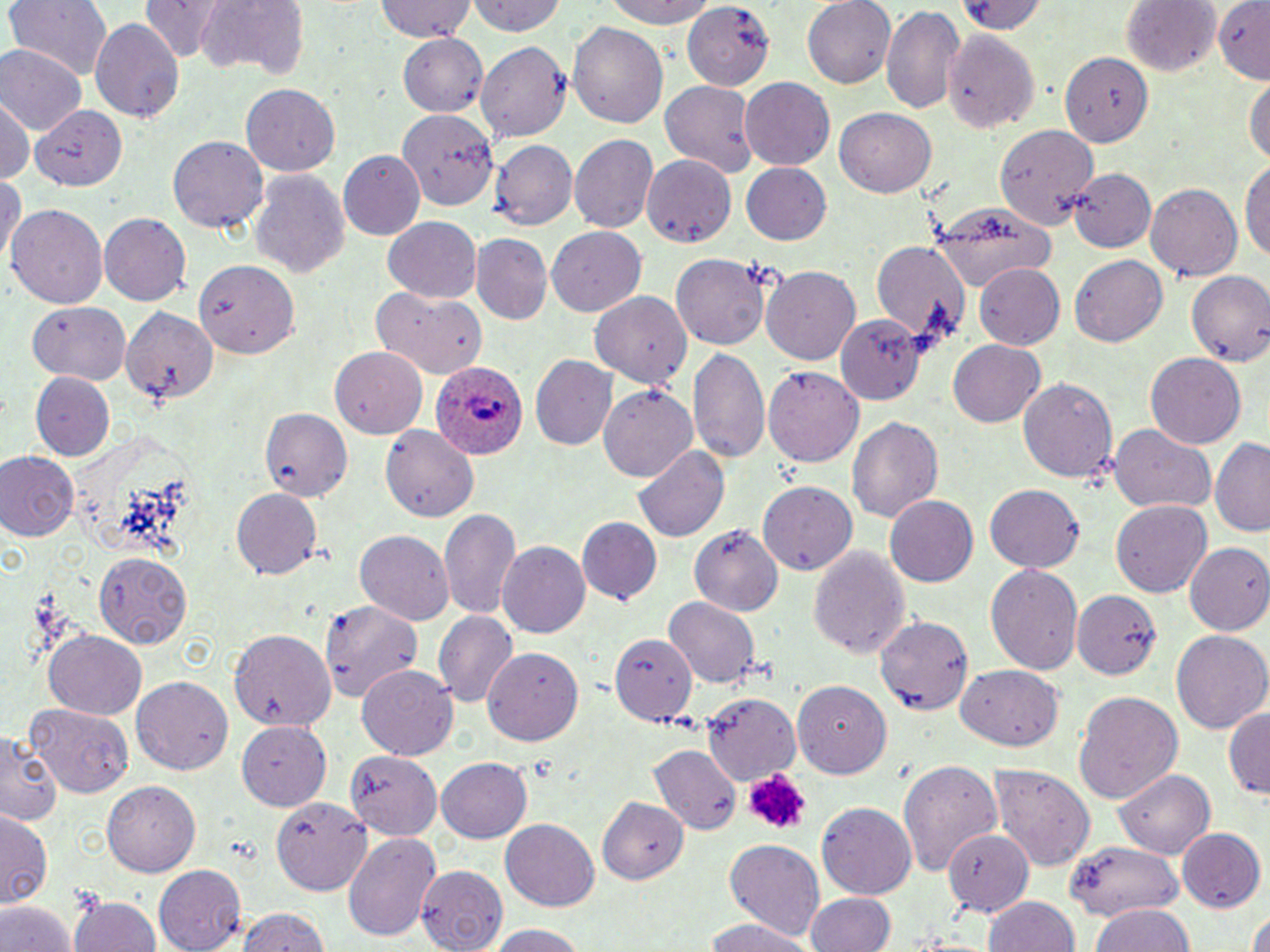

Summary:
  - Coordinate format: approximate bounding boxes as named x1/y1/x2/y2 corners in pixels
  - Plasmodium ovale-infected red blood cell locations: (x1=428, y1=355, x2=528, y2=462)
  - Platelet locations: (x1=739, y1=767, x2=811, y2=835)
  - Uninfected red blood cell locations: (x1=3, y1=0, x2=111, y2=81), (x1=373, y1=0, x2=477, y2=43), (x1=597, y1=0, x2=726, y2=28), (x1=802, y1=0, x2=896, y2=89), (x1=957, y1=0, x2=1053, y2=36), (x1=1212, y1=0, x2=1270, y2=82), (x1=468, y1=1, x2=570, y2=38), (x1=682, y1=1, x2=771, y2=87), (x1=1121, y1=1, x2=1218, y2=78), (x1=142, y1=2, x2=226, y2=61), (x1=193, y1=3, x2=303, y2=80), (x1=880, y1=6, x2=966, y2=116), (x1=90, y1=17, x2=184, y2=125), (x1=569, y1=20, x2=668, y2=130), (x1=942, y1=24, x2=1040, y2=131), (x1=399, y1=36, x2=491, y2=114), (x1=479, y1=42, x2=572, y2=142), (x1=0, y1=45, x2=83, y2=136), (x1=1055, y1=47, x2=1155, y2=150), (x1=1246, y1=73, x2=1269, y2=174), (x1=739, y1=77, x2=833, y2=167), (x1=662, y1=80, x2=757, y2=178), (x1=241, y1=82, x2=342, y2=174), (x1=0, y1=96, x2=33, y2=184), (x1=31, y1=103, x2=128, y2=189), (x1=399, y1=106, x2=498, y2=214), (x1=834, y1=109, x2=936, y2=198), (x1=992, y1=123, x2=1099, y2=234), (x1=568, y1=136, x2=656, y2=234), (x1=168, y1=137, x2=268, y2=235), (x1=490, y1=140, x2=576, y2=229), (x1=339, y1=150, x2=427, y2=240), (x1=644, y1=157, x2=737, y2=245), (x1=1241, y1=160, x2=1269, y2=261), (x1=740, y1=161, x2=832, y2=244), (x1=1068, y1=166, x2=1157, y2=251), (x1=0, y1=171, x2=24, y2=270), (x1=249, y1=171, x2=349, y2=279), (x1=1147, y1=182, x2=1242, y2=283), (x1=929, y1=201, x2=1055, y2=288), (x1=7, y1=203, x2=108, y2=308), (x1=100, y1=212, x2=194, y2=305), (x1=384, y1=217, x2=482, y2=303), (x1=546, y1=227, x2=644, y2=316), (x1=472, y1=234, x2=551, y2=324), (x1=870, y1=238, x2=969, y2=347), (x1=1070, y1=252, x2=1168, y2=344), (x1=673, y1=254, x2=770, y2=349), (x1=196, y1=262, x2=301, y2=360), (x1=975, y1=265, x2=1065, y2=350), (x1=760, y1=266, x2=861, y2=365), (x1=1186, y1=270, x2=1270, y2=367), (x1=590, y1=291, x2=692, y2=386), (x1=382, y1=293, x2=489, y2=381), (x1=29, y1=300, x2=130, y2=383), (x1=118, y1=305, x2=216, y2=414), (x1=831, y1=315, x2=923, y2=402), (x1=948, y1=340, x2=1045, y2=428), (x1=328, y1=347, x2=427, y2=438), (x1=688, y1=348, x2=768, y2=462), (x1=1144, y1=352, x2=1247, y2=450), (x1=532, y1=355, x2=618, y2=452), (x1=765, y1=366, x2=864, y2=467), (x1=30, y1=373, x2=115, y2=461), (x1=1018, y1=377, x2=1118, y2=485), (x1=599, y1=383, x2=699, y2=482), (x1=262, y1=405, x2=357, y2=502), (x1=846, y1=416, x2=943, y2=528), (x1=382, y1=423, x2=480, y2=523), (x1=1109, y1=426, x2=1218, y2=515), (x1=1211, y1=436, x2=1270, y2=538), (x1=633, y1=445, x2=729, y2=543), (x1=0, y1=450, x2=79, y2=541), (x1=758, y1=480, x2=859, y2=576), (x1=986, y1=484, x2=1085, y2=573), (x1=231, y1=489, x2=322, y2=580), (x1=886, y1=495, x2=978, y2=588), (x1=1112, y1=501, x2=1212, y2=597), (x1=439, y1=508, x2=521, y2=620), (x1=579, y1=518, x2=661, y2=604), (x1=690, y1=522, x2=785, y2=615), (x1=357, y1=530, x2=455, y2=624), (x1=806, y1=542, x2=912, y2=662), (x1=499, y1=543, x2=591, y2=637), (x1=1185, y1=543, x2=1270, y2=634), (x1=94, y1=553, x2=193, y2=647), (x1=985, y1=565, x2=1083, y2=675), (x1=1074, y1=589, x2=1161, y2=681), (x1=664, y1=595, x2=760, y2=690), (x1=321, y1=601, x2=426, y2=705), (x1=433, y1=609, x2=517, y2=709), (x1=876, y1=614, x2=975, y2=712), (x1=229, y1=628, x2=334, y2=731), (x1=1171, y1=629, x2=1269, y2=736), (x1=43, y1=632, x2=148, y2=721), (x1=611, y1=634, x2=696, y2=722), (x1=482, y1=644, x2=583, y2=743), (x1=358, y1=665, x2=459, y2=763), (x1=955, y1=666, x2=1064, y2=751), (x1=788, y1=675, x2=893, y2=781), (x1=133, y1=678, x2=231, y2=776), (x1=1074, y1=692, x2=1183, y2=805), (x1=703, y1=693, x2=801, y2=782), (x1=27, y1=704, x2=133, y2=797), (x1=1224, y1=705, x2=1269, y2=801), (x1=236, y1=721, x2=330, y2=810), (x1=0, y1=730, x2=62, y2=829), (x1=648, y1=744, x2=742, y2=834), (x1=341, y1=747, x2=447, y2=841), (x1=436, y1=757, x2=532, y2=844), (x1=896, y1=758, x2=1004, y2=879), (x1=992, y1=763, x2=1095, y2=869), (x1=1113, y1=769, x2=1216, y2=859), (x1=101, y1=782, x2=197, y2=877), (x1=269, y1=795, x2=371, y2=896), (x1=594, y1=796, x2=686, y2=878), (x1=817, y1=802, x2=915, y2=900), (x1=1, y1=809, x2=54, y2=905), (x1=501, y1=819, x2=598, y2=911), (x1=946, y1=828, x2=1031, y2=913), (x1=1176, y1=829, x2=1264, y2=913), (x1=344, y1=831, x2=438, y2=942), (x1=722, y1=840, x2=825, y2=939), (x1=1067, y1=840, x2=1182, y2=930), (x1=416, y1=865, x2=509, y2=952), (x1=153, y1=866, x2=243, y2=950), (x1=70, y1=892, x2=162, y2=952), (x1=805, y1=892, x2=896, y2=952), (x1=982, y1=896, x2=1080, y2=952), (x1=0, y1=898, x2=76, y2=952), (x1=1089, y1=904, x2=1199, y2=952), (x1=236, y1=906, x2=331, y2=952), (x1=1244, y1=912, x2=1270, y2=952), (x1=701, y1=918, x2=813, y2=952), (x1=484, y1=923, x2=591, y2=952)
  - Slide-level diagnosis: Plasmodium ovale
  - Field of view: single
  - Stain: May-Grünwald-Giemsa
  - Magnification: 1000x
  - Image size: 1270×952 pixels
  - Preparation: thin blood film
  - Modality: light microscopy